Name the cell type shown.
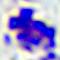
A leukocyte.

Summary:
  - Modality: photomicrograph
  - Magnification: 400x